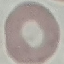

Result: no malaria parasites detected. Thin smear of blood. Giemsa-stained preparation. Acquired by smartphone through the microscope eyepiece. Cell patch, automatically extracted from a larger field of view and resized to 64 × 64 pixels.